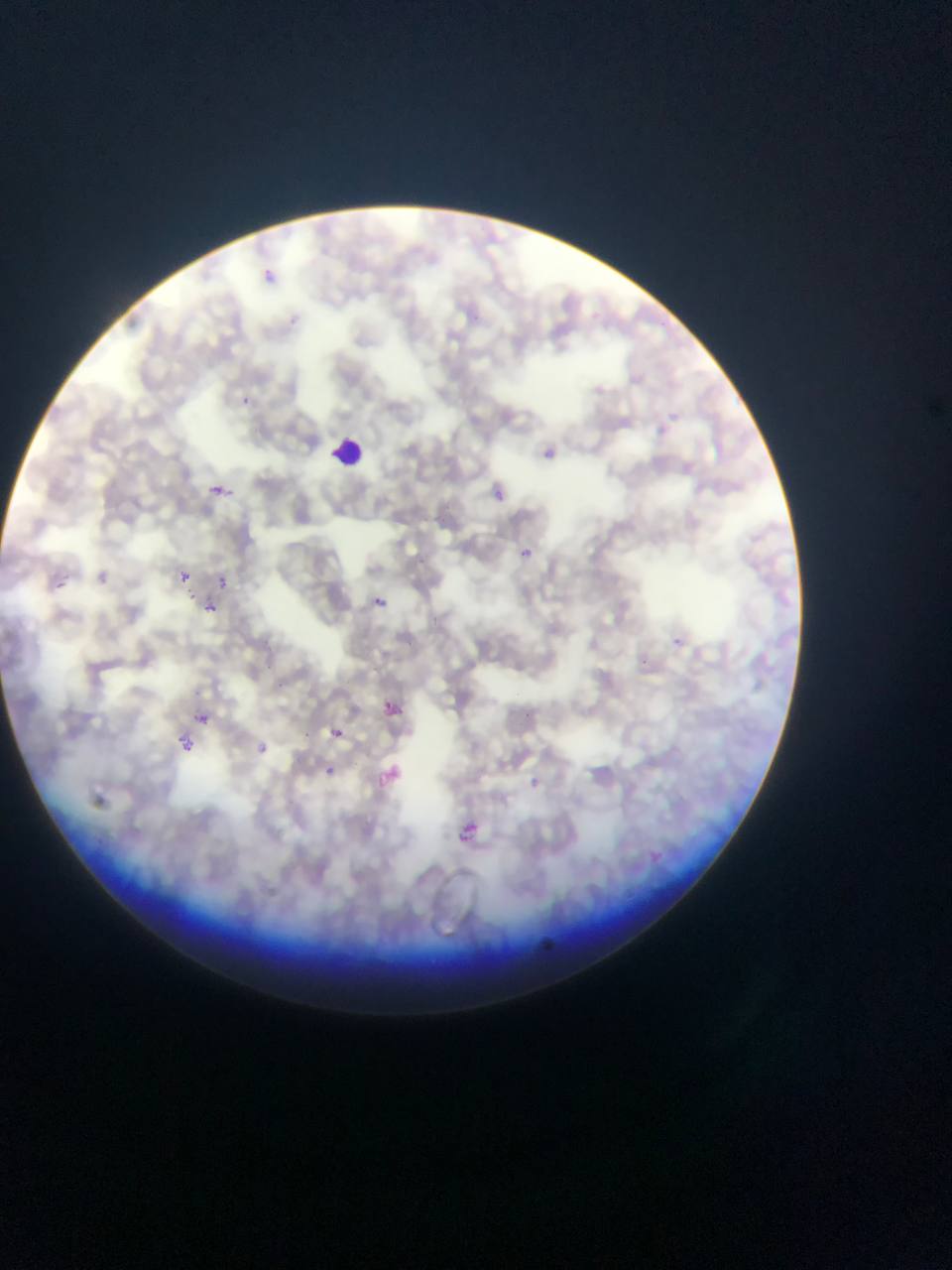
Approximate bounding boxes as [left, top, right, bottom] in pixels. Leukocyte locations: [329, 433, 367, 471]. Plasmodium parasite locations: [255, 265, 280, 289], [537, 439, 561, 467], [204, 481, 232, 504], [489, 484, 510, 503], [518, 545, 537, 562], [52, 566, 70, 594], [174, 568, 193, 586], [94, 569, 110, 586], [214, 574, 231, 591], [363, 591, 392, 613], [201, 601, 218, 616], [378, 699, 401, 723], [197, 714, 218, 729], [324, 723, 349, 746], [171, 735, 194, 758], [247, 737, 275, 763], [321, 762, 340, 780], [374, 762, 405, 790], [529, 777, 545, 791], [453, 819, 487, 853], [530, 936, 558, 952]. Sample from Ghana. Image is 952×1270 pixels. Thin blood smear. One field of view. Mobile-phone photograph taken through the microscope.